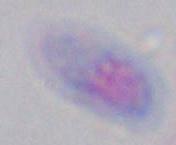

Summary:
  - Magnification: 1000x
  - Identification: Toxoplasma gondii
  - Modality: micrograph